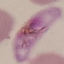 Result: malaria parasites identified. Giemsa stain. Thin blood smear. Acquired by smartphone through the microscope eyepiece. Cell patch, automatically extracted from a larger field of view and resized to 64 × 64 pixels.